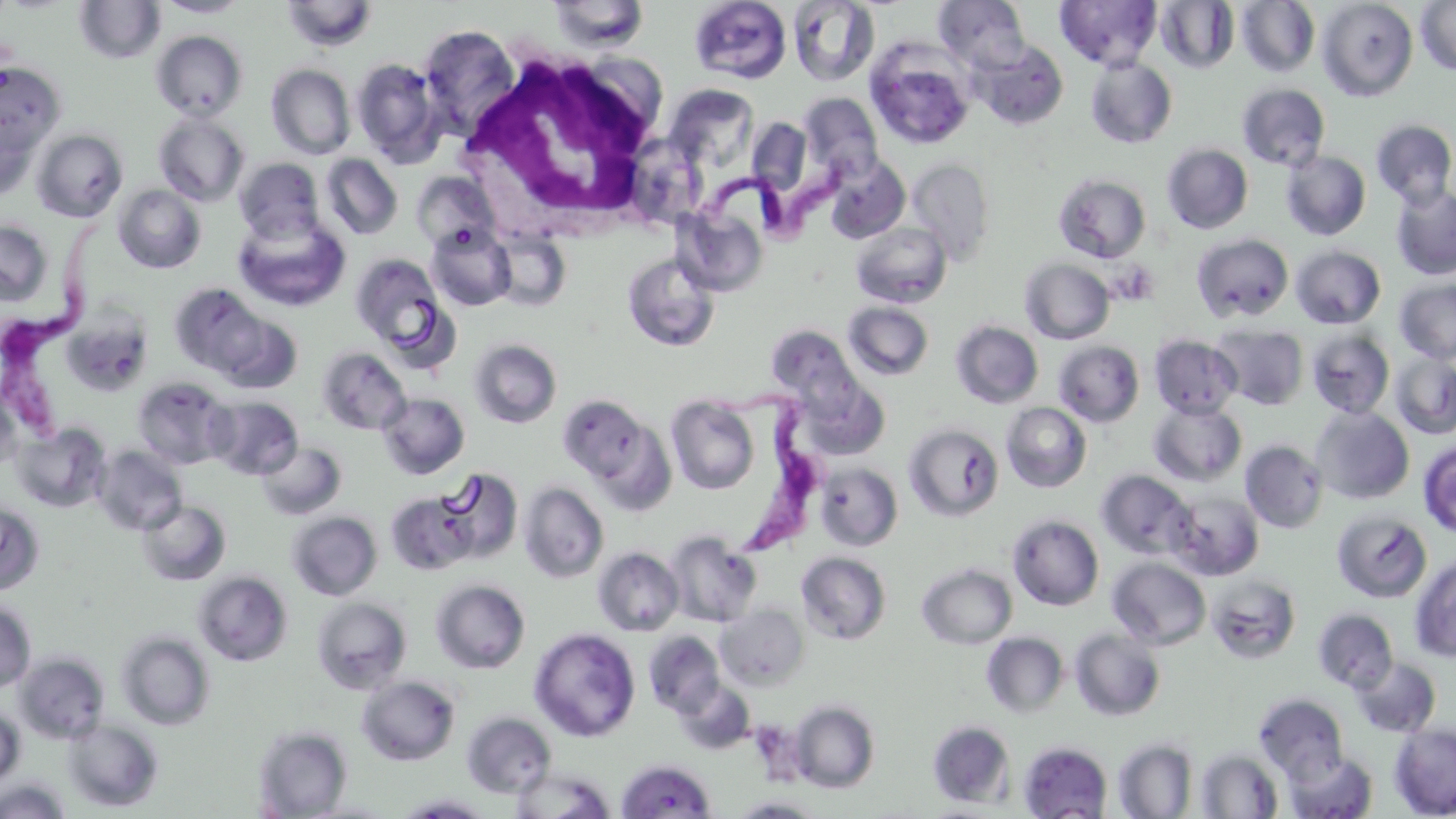

trypanosoma_brucei_locations: 'approximate bounding boxes as (x1, y1, x2, y2) in pixels: (670, 140, 865, 246), (3, 216, 122, 444), (704, 389, 819, 553)'
slide_level_diagnosis: Trypanosoma brucei
preparation: thin blood smear
white_blood_cell_locations: 'approximate bounding boxes as (x1, y1, x2, y2) in pixels: (459, 48, 666, 233)'
uninfected_red_blood_cell_locations: 'approximate bounding boxes as (x1, y1, x2, y2) in pixels: (154, 0, 251, 18), (689, 0, 792, 83), (787, 0, 879, 86), (933, 0, 1031, 74), (1236, 0, 1320, 77), (1317, 0, 1418, 101), (74, 1, 166, 64), (280, 1, 379, 53), (547, 1, 651, 53), (1055, 1, 1162, 71), (1156, 1, 1240, 73), (1415, 1, 1456, 76), (418, 24, 520, 137), (151, 30, 248, 121), (863, 38, 976, 150), (973, 41, 1068, 129), (1086, 57, 1178, 148), (2, 58, 64, 164), (351, 58, 445, 165), (266, 64, 355, 159), (1237, 83, 1331, 170), (673, 93, 755, 172), (799, 93, 883, 179), (0, 108, 37, 200), (153, 112, 250, 206), (747, 117, 813, 198), (1372, 119, 1456, 208), (31, 129, 128, 222), (1162, 144, 1253, 234), (1281, 151, 1371, 241), (321, 154, 403, 239), (824, 155, 910, 243), (234, 157, 325, 243), (908, 158, 996, 265), (320, 160, 502, 244), (412, 171, 501, 253), (1053, 173, 1151, 263), (1390, 184, 1456, 280), (113, 185, 206, 273), (676, 204, 770, 296), (235, 214, 350, 312), (0, 220, 52, 305), (850, 222, 952, 308), (426, 224, 517, 311), (1192, 234, 1294, 322), (1291, 245, 1386, 329), (350, 253, 450, 352), (622, 253, 720, 352), (1020, 258, 1114, 344), (1395, 278, 1456, 364), (169, 283, 268, 376), (842, 302, 934, 381), (210, 310, 303, 394), (950, 321, 1043, 408), (765, 324, 860, 406), (1211, 325, 1308, 409), (1307, 329, 1395, 418), (1149, 334, 1242, 419), (469, 339, 562, 428), (1053, 340, 1145, 427), (317, 347, 411, 435), (1390, 353, 1456, 439), (133, 376, 234, 469), (0, 380, 21, 471), (378, 392, 470, 479), (558, 394, 660, 492), (665, 395, 760, 495), (206, 396, 303, 479), (1149, 401, 1247, 486), (1002, 402, 1091, 492), (1311, 406, 1414, 504), (13, 423, 110, 512), (904, 423, 1004, 522), (1240, 439, 1328, 533), (1419, 440, 1456, 539), (256, 441, 347, 521), (93, 445, 187, 536), (815, 462, 903, 551), (435, 468, 523, 563), (1096, 469, 1196, 560), (519, 481, 609, 583), (386, 491, 480, 576), (1169, 491, 1264, 581), (138, 500, 231, 586), (0, 501, 43, 594), (286, 511, 382, 601), (1333, 511, 1432, 602), (1007, 514, 1104, 611), (664, 530, 762, 627), (593, 547, 684, 636), (796, 551, 892, 645), (1108, 557, 1211, 650), (1410, 558, 1456, 662), (917, 563, 1017, 649), (193, 571, 292, 666), (1206, 574, 1302, 665), (430, 579, 530, 674), (311, 597, 412, 694), (0, 600, 36, 692), (716, 604, 809, 691), (1313, 608, 1399, 693), (530, 628, 641, 742), (1070, 629, 1166, 721), (116, 631, 215, 730), (644, 631, 726, 717), (981, 632, 1069, 718), (15, 648, 217, 739), (14, 653, 111, 743), (1352, 656, 1441, 737), (357, 675, 460, 766), (675, 681, 757, 756), (1254, 694, 1348, 782), (788, 700, 880, 793), (0, 708, 24, 789), (461, 712, 556, 799), (64, 719, 163, 811), (927, 721, 1015, 808), (1389, 723, 1456, 818), (253, 726, 352, 818), (1113, 739, 1197, 818), (1018, 741, 1113, 818), (1197, 749, 1283, 818), (1284, 750, 1378, 819), (616, 759, 717, 818), (512, 769, 616, 818), (0, 778, 71, 819), (392, 794, 496, 818), (726, 796, 827, 818)'
modality: light microscopy
field_of_view: one of a larger specimen
stain: May-Grünwald-Giemsa
image_size: 1456×819 pixels
magnification: 1000x